Assess this cell for malaria.
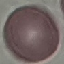

Uninfected.

Summary:
  - Capture: smartphone camera at the microscope eyepiece
  - Image type: cell patch, automatically extracted from a larger field of view and resized to 64 × 64 pixels
  - Preparation: thin blood film
  - Stain: Giemsa